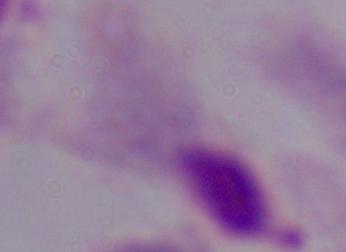

modality = micrograph
identification = trichomonad
magnification = 1000x